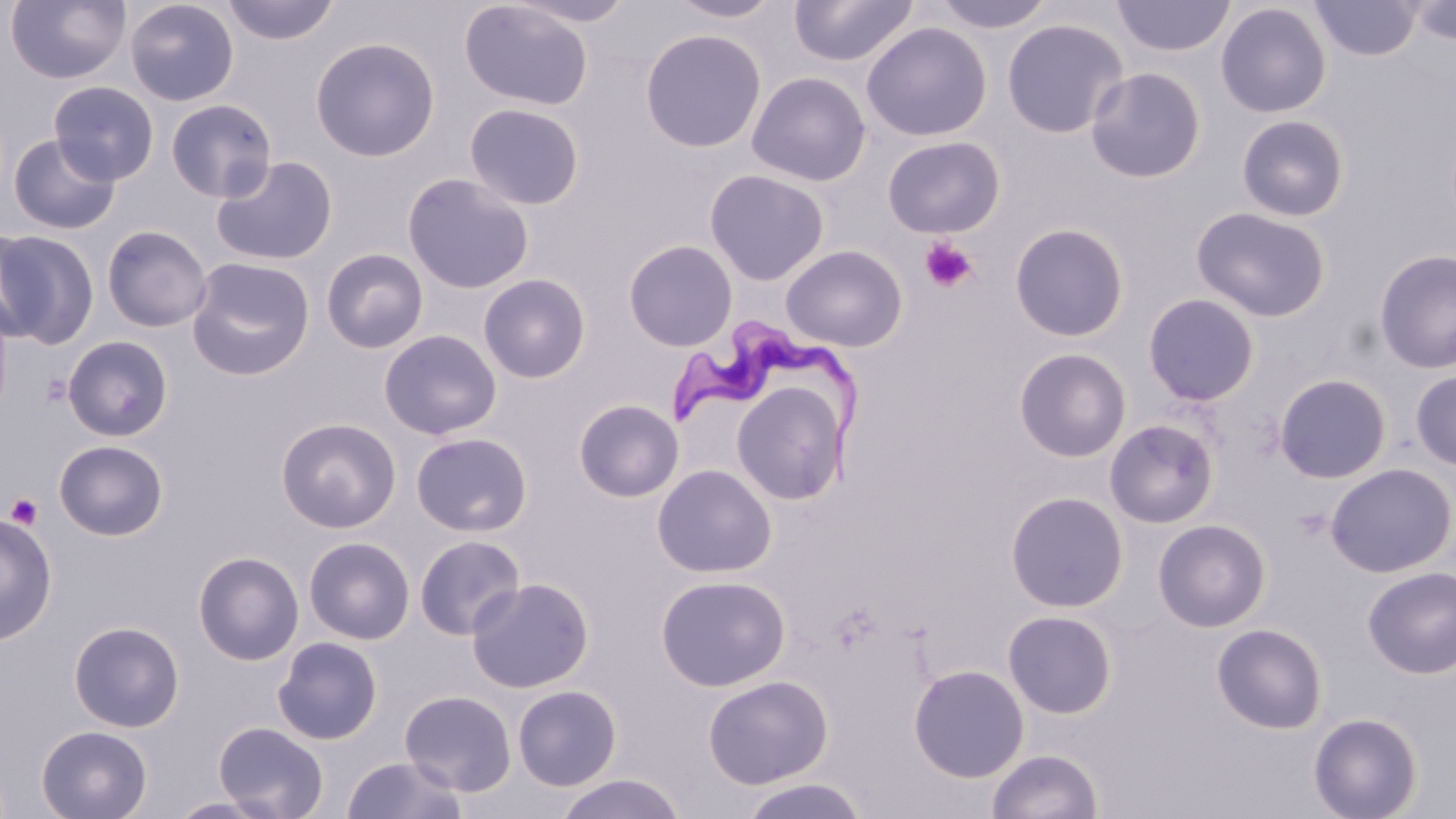
Trypanosoma brucei locations = approximate bounding boxes as (x1,y1)-(x2,y2) corner pairs in pixels: (668,318)-(861,483)
slide-level diagnosis = Trypanosoma brucei
modality = optical microscopy
preparation = thin blood smear
field of view = single
uninfected red blood cell locations = approximate bounding boxes as (x1,y1)-(x2,y2) corner pairs in pixels: (5,0)-(131,84), (125,0)-(239,106), (220,0)-(340,46), (506,0)-(639,27), (666,0)-(787,23), (788,0)-(918,67), (929,0)-(1058,33), (1111,0)-(1235,58), (1310,0)-(1421,61), (459,1)-(594,111), (1406,1)-(1456,46), (1215,2)-(1332,118), (1001,18)-(1129,139), (861,22)-(993,142), (640,28)-(767,153), (310,37)-(440,162), (1085,66)-(1207,183), (746,71)-(871,187), (48,81)-(160,185), (166,99)-(277,202), (464,103)-(585,210), (1235,114)-(1350,222), (8,133)-(120,234), (882,136)-(1005,238), (210,155)-(338,266), (704,168)-(829,286), (402,173)-(536,294), (1190,206)-(1331,322), (1009,222)-(1129,342), (102,225)-(212,332), (0,227)-(44,347), (0,229)-(100,350), (623,239)-(738,351), (780,244)-(908,351), (321,248)-(429,354), (1373,249)-(1456,374), (187,257)-(315,380), (478,273)-(591,383), (1142,292)-(1261,407), (0,298)-(14,424), (379,329)-(503,440), (62,335)-(173,441), (1012,347)-(1132,462), (1409,369)-(1456,471), (1274,373)-(1392,483), (731,381)-(850,504), (573,398)-(684,502), (276,417)-(401,534), (1103,419)-(1220,530), (411,432)-(533,537), (53,439)-(169,541), (1325,462)-(1456,578), (651,464)-(777,578), (1005,490)-(1129,612), (0,511)-(58,646), (1152,519)-(1271,632), (414,535)-(525,640), (304,536)-(415,644), (192,551)-(305,666), (1362,566)-(1456,678), (655,574)-(791,691), (466,577)-(594,693), (1002,609)-(1118,718), (68,621)-(185,733), (1211,623)-(1328,734), (272,636)-(383,745), (908,664)-(1030,782), (702,674)-(834,790), (513,684)-(622,791), (399,690)-(517,796), (1307,711)-(1424,819), (213,721)-(329,819), (36,724)-(153,818), (986,748)-(1103,819), (342,754)-(467,818), (555,773)-(685,819), (738,777)-(869,819), (165,794)-(285,818)
stain = May-Grünwald-Giemsa
image size = 1456×819 pixels
magnification = 1000x
platelet locations = approximate bounding boxes as (x1,y1)-(x2,y2) corner pairs in pixels: (919,237)-(978,293), (40,372)-(73,407), (5,493)-(44,529)